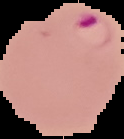

Summary:
  - Result: malaria parasites detected
  - Image type: segmented cell region with the area outside set to black
  - Preparation: thin blood film
  - Image size: 124×139 pixels